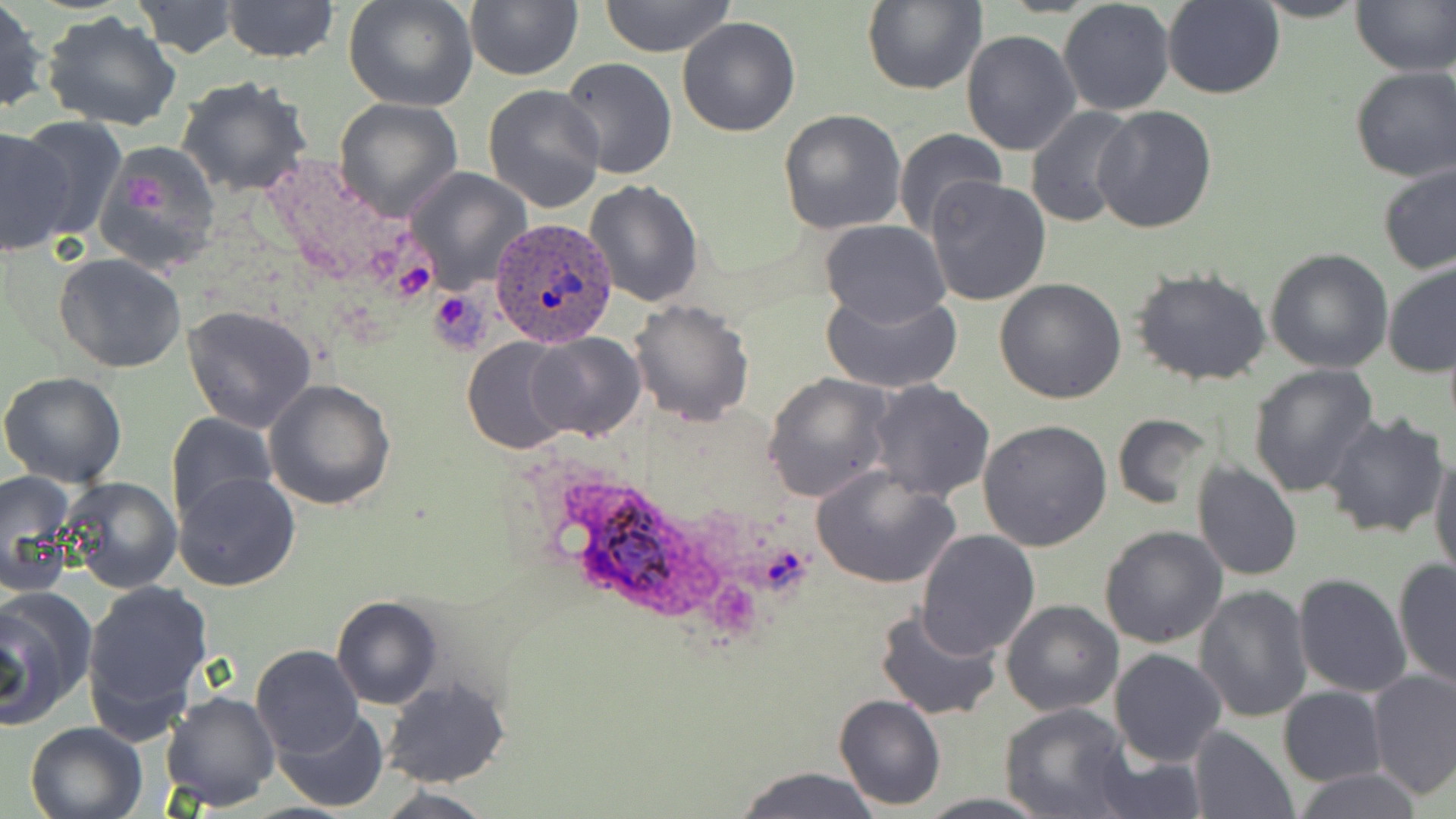
Summary:
  - Coordinate format: approximate bounding boxes as (x1,y1)-(x2,y2) corner pairs in pixels
  - Plasmodium ovale-infected red blood cell locations: (491,217)-(617,349), (566,484)-(699,611)
  - Platelet locations: (119,168)-(169,217), (389,259)-(439,300)
  - Uninfected red blood cell locations: (0,0)-(48,113), (342,0)-(479,113), (463,0)-(581,82), (598,0)-(735,56), (863,0)-(985,94), (1248,0)-(1369,22), (1349,0)-(1456,76), (130,1)-(240,58), (222,1)-(338,65), (1059,1)-(1175,116), (1161,1)-(1287,99), (41,12)-(183,132), (677,16)-(801,137), (961,29)-(1082,156), (560,56)-(676,179), (1349,66)-(1456,182), (175,76)-(314,198), (482,84)-(607,215), (333,97)-(464,222), (1092,104)-(1219,232), (1024,106)-(1140,228), (778,109)-(908,233), (0,123)-(92,252), (892,128)-(1006,242), (94,142)-(222,275), (1376,160)-(1456,275), (402,167)-(532,293), (926,177)-(1051,306), (583,178)-(706,306), (819,220)-(949,327), (1265,247)-(1395,373), (55,253)-(187,372), (1381,259)-(1456,378), (1131,268)-(1275,388), (993,278)-(1126,405), (821,287)-(962,392), (628,299)-(755,424), (181,305)-(319,433), (525,331)-(645,442), (463,337)-(577,454), (1249,364)-(1380,499), (0,371)-(128,488), (763,372)-(893,502), (867,377)-(997,502), (264,378)-(396,510), (1320,410)-(1451,540), (165,411)-(278,525), (1112,413)-(1215,512), (978,420)-(1112,552), (1429,445)-(1455,581), (1191,461)-(1304,583), (811,465)-(961,588), (2,470)-(77,596), (174,472)-(301,593), (57,477)-(182,594), (1098,526)-(1228,648), (915,529)-(1040,661), (1393,560)-(1455,690), (1293,573)-(1414,698), (80,578)-(213,731), (1194,584)-(1313,723), (0,585)-(96,723), (331,595)-(443,709), (1001,601)-(1124,716), (873,606)-(1002,720), (251,645)-(364,758), (1109,648)-(1227,766), (1365,668)-(1456,799), (379,679)-(512,787), (1278,687)-(1386,786), (161,690)-(280,812), (832,693)-(947,810), (1000,703)-(1135,818), (273,707)-(389,812), (24,719)-(149,819), (1188,726)-(1299,819), (1088,742)-(1207,818), (732,767)-(882,819), (1289,768)-(1423,819), (375,787)-(496,819), (914,794)-(1053,819)
  - Slide-level diagnosis: Plasmodium ovale
  - Modality: optical microscopy
  - Stain: May-Grünwald-Giemsa
  - Preparation: thin blood film
  - Field of view: single
  - Magnification: 1000x
  - Image size: 1456×819 pixels